Assess this cell for malaria.
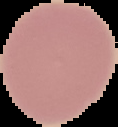

It is uninfected.

preparation = thin blood smear
image size = 118×127 pixels
image type = cell region segmented out of the field of view; surrounding area masked to black